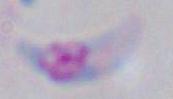

magnification: 1000x
identification: Toxoplasma gondii
modality: micrograph